Locate every blood parasite and identify its species.
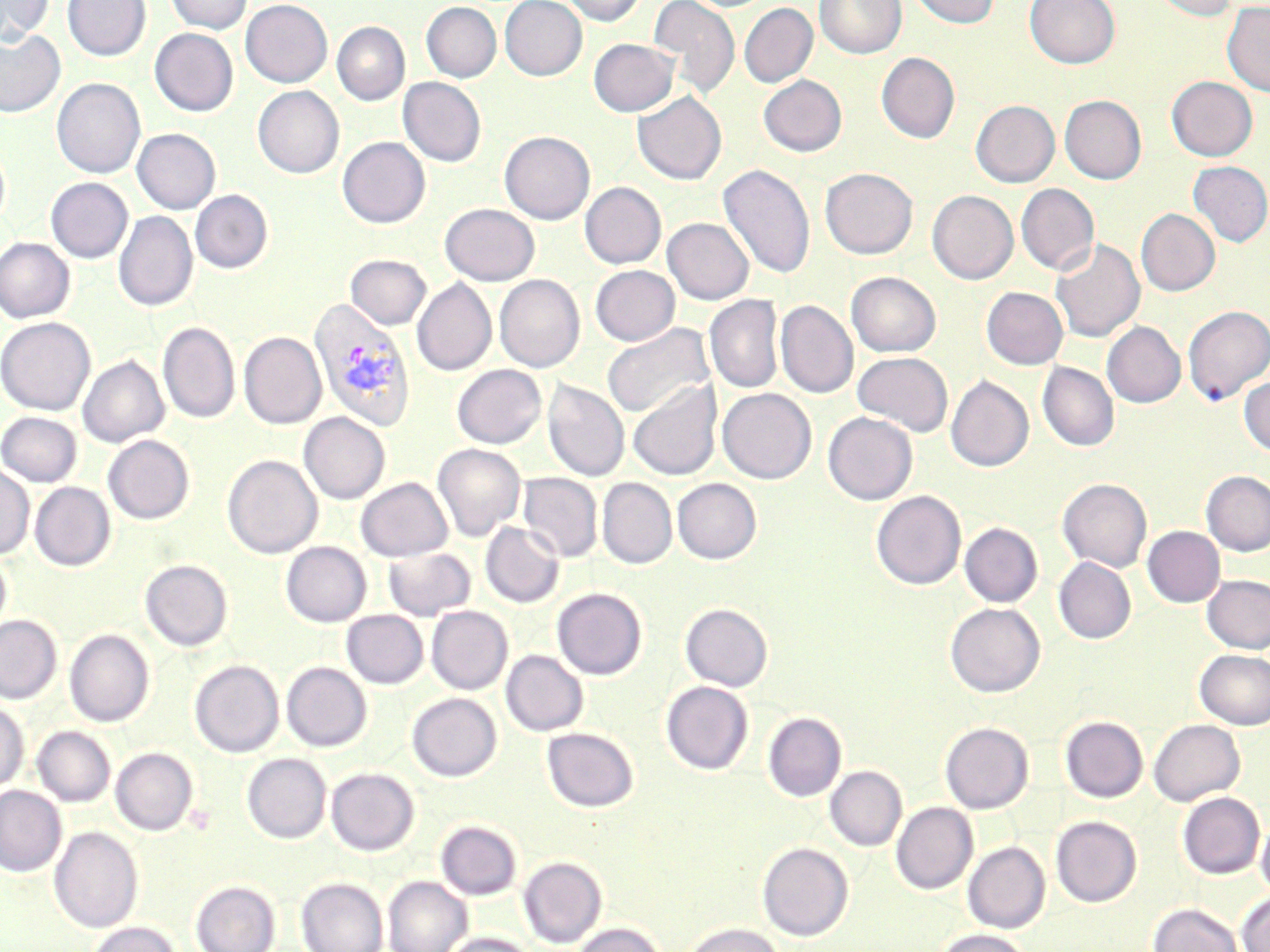
Approximate bounding boxes as (x1,y1)-(x2,y2) corner pairs in pixels.
Plasmodium vivax-infected red blood cells: (309,298)-(416,431).
No Plasmodium falciparum, Plasmodium ovale, Plasmodium malariae, Babesia divergens, or Trypanosoma brucei observed.

Summary:
  - Uninfected red blood cell locations: (0,0)-(54,45), (62,0)-(151,61), (166,0)-(252,34), (241,0)-(332,87), (500,0)-(587,80), (559,0)-(646,26), (648,0)-(740,99), (815,0)-(907,59), (908,0)-(1000,29), (1025,0)-(1120,69), (1149,0)-(1240,21), (1222,1)-(1270,97), (421,2)-(501,82), (739,3)-(818,87), (332,21)-(409,105), (0,28)-(65,118), (150,28)-(238,116), (589,38)-(679,116), (876,52)-(960,143), (758,75)-(847,156), (1166,76)-(1257,161), (398,77)-(486,166), (52,78)-(146,178), (253,85)-(344,178), (632,91)-(726,185), (1060,95)-(1146,184), (971,100)-(1060,187), (132,128)-(220,214), (500,131)-(595,225), (338,137)-(430,228), (1187,161)-(1270,246), (718,164)-(815,279), (820,167)-(918,259), (46,177)-(133,263), (580,182)-(666,269), (1016,184)-(1100,275), (190,190)-(273,273), (927,190)-(1018,284), (440,203)-(540,285), (1136,208)-(1220,296), (114,211)-(198,312), (663,218)-(754,304), (0,237)-(75,323), (1050,238)-(1145,343), (346,254)-(431,329), (590,265)-(679,346), (846,271)-(941,357), (494,275)-(585,372), (412,278)-(496,376), (981,287)-(1068,369), (704,295)-(783,394), (776,300)-(858,398), (1183,305)-(1270,404), (0,317)-(95,415), (158,322)-(240,423), (1102,322)-(1186,407), (601,323)-(715,419), (239,332)-(326,429), (852,352)-(953,436), (78,355)-(169,447), (1037,361)-(1119,452), (452,364)-(546,448), (946,375)-(1034,472), (1239,376)-(1270,456), (543,380)-(630,482), (628,381)-(722,480), (717,388)-(816,484), (0,411)-(82,487), (299,412)-(390,503), (823,412)-(918,504), (103,435)-(194,524), (432,443)-(526,541), (222,454)-(323,558), (0,462)-(34,560), (1201,471)-(1270,556), (518,473)-(602,562), (355,477)-(452,561), (597,478)-(677,568), (672,478)-(761,563), (1058,478)-(1152,572), (30,482)-(115,571), (871,490)-(965,590), (481,521)-(565,607), (960,523)-(1042,607), (1142,526)-(1225,607), (281,541)-(371,627), (383,546)-(476,621), (0,549)-(11,637), (1054,556)-(1136,644), (140,559)-(233,651), (1202,575)-(1270,654), (552,587)-(647,679), (945,602)-(1045,697), (680,603)-(773,691), (426,606)-(512,694), (341,610)-(428,688), (0,615)-(62,704), (64,629)-(154,727), (1195,649)-(1270,729), (501,650)-(588,736), (189,660)-(284,757), (282,662)-(371,751), (661,681)-(753,774), (407,693)-(501,781), (0,700)-(29,793), (763,712)-(846,801), (1060,716)-(1148,802), (1148,719)-(1245,805), (940,721)-(1034,814), (32,726)-(115,807), (542,727)-(638,812), (111,747)-(198,835), (242,753)-(331,843), (825,766)-(906,850), (326,767)-(419,855), (0,785)-(66,877), (1178,792)-(1265,878), (891,802)-(977,893), (1256,814)-(1270,897), (1051,816)-(1142,906), (436,820)-(522,900), (49,825)-(143,933), (963,841)-(1050,933), (757,842)-(853,941), (519,856)-(606,947), (383,876)-(472,952), (297,877)-(388,952), (191,880)-(280,952), (1236,891)-(1270,952), (1148,902)-(1244,952), (87,921)-(180,952), (573,922)-(666,952), (683,923)-(784,952), (935,928)-(1032,952), (441,933)-(537,952)
  - Slide-level diagnosis: Plasmodium vivax
  - Stain: May-Grünwald-Giemsa
  - Magnification: 1000x
  - Image size: 1270×952 pixels
  - Field of view: one of a larger specimen
  - Modality: optical microscopy
  - Preparation: thin blood film